Assess this cell for malaria.
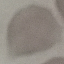
It is uninfected.

stain = Giemsa
image type = cell patch, automatically extracted from a larger field of view and resized to 64 × 64 pixels
preparation = thin blood smear
capture = smartphone camera at the microscope eyepiece